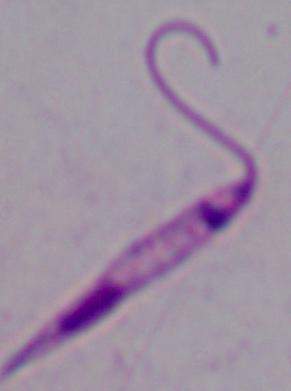
A Leishmania parasite is seen. Photomicrograph. Captured at 1000x magnification.